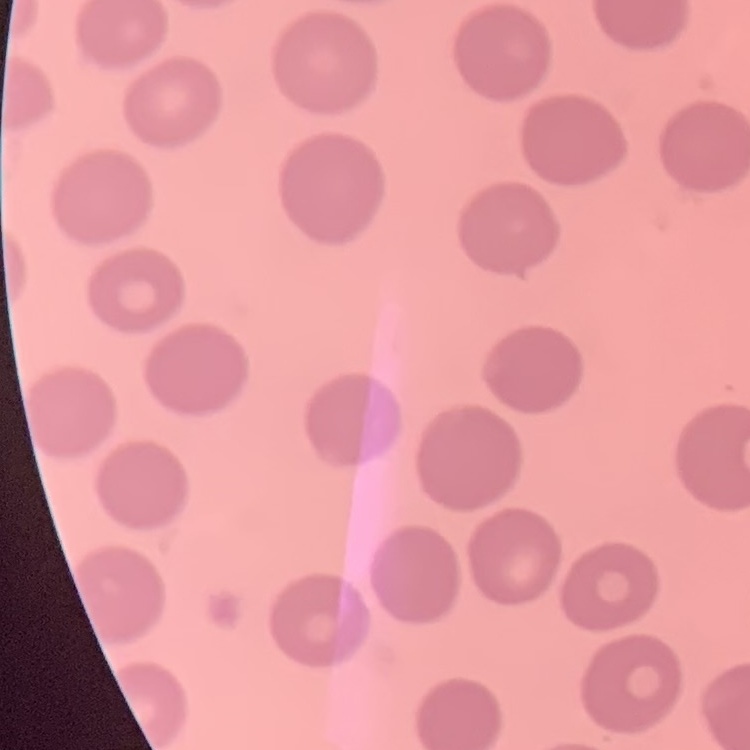 The erythrocytes show no rouleaux formation. Square crop of a larger photomicrograph. Thin peripheral smear. Field's or Giemsa stain.